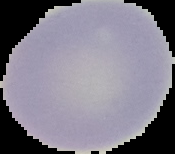

Summary:
  - Result: negative for malaria parasites
  - Image size: 175×154 pixels
  - Image type: cell region segmented out of the field of view; surrounding area masked to black
  - Preparation: thin blood smear